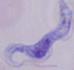

Summary:
  - Magnification: 1000x
  - Modality: micrograph
  - Identification: trypanosome